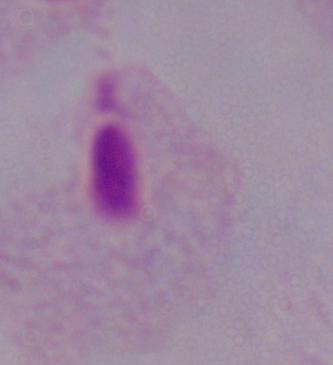
Summary:
  - Identification: trichomonad
  - Modality: photomicrograph
  - Magnification: 1000x